Mark where platelets are.
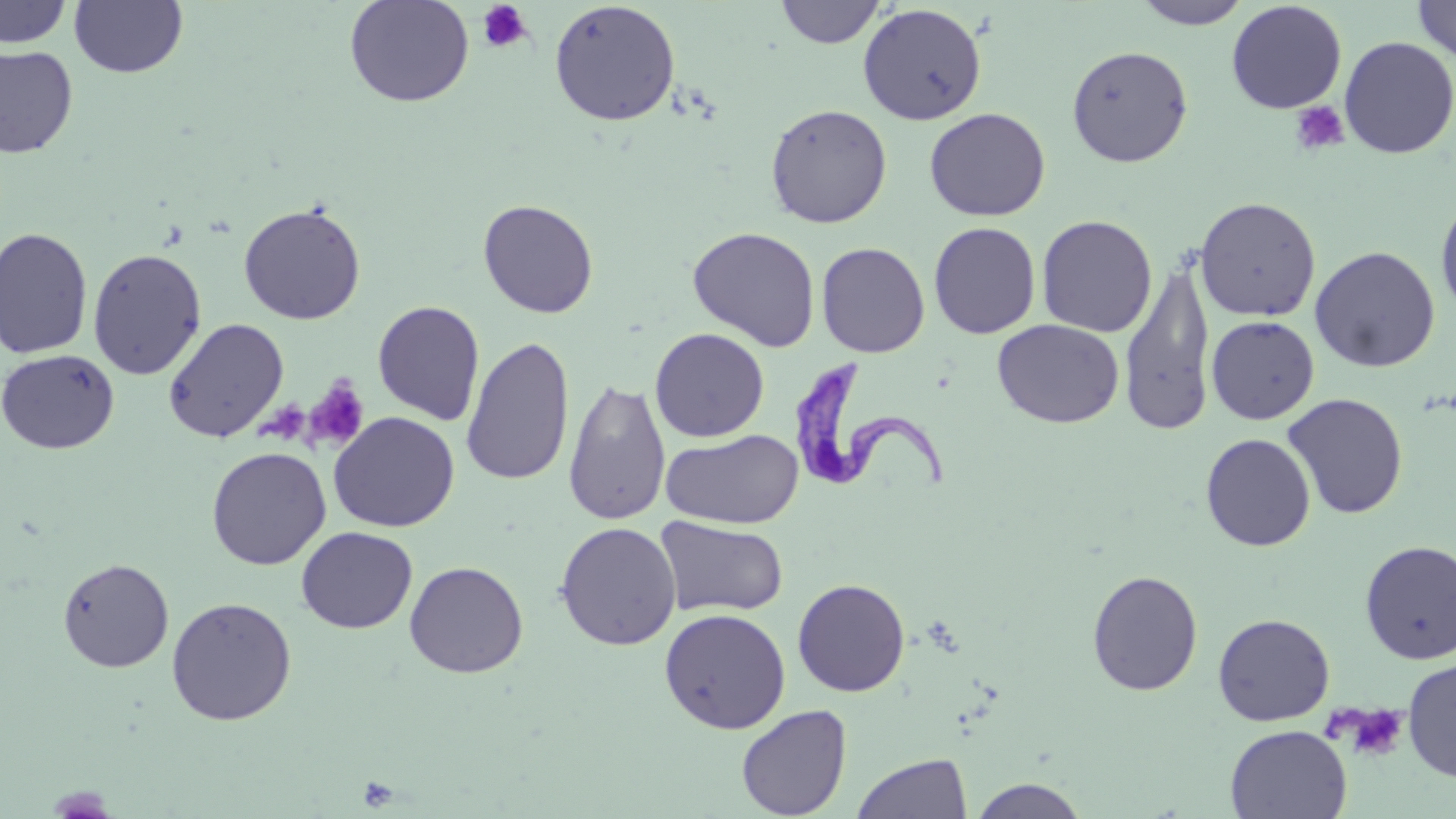

Approximate bounding boxes as [x1, y1, x2, y2] in pixels.
Platelets: [476, 1, 534, 53], [1290, 101, 1350, 156], [303, 378, 370, 452], [1339, 704, 1409, 761].

Summary:
  - Uninfected red blood cell locations: [343, 0, 475, 108], [1131, 0, 1253, 29], [1412, 0, 1456, 64], [0, 1, 73, 49], [69, 1, 188, 78], [549, 1, 680, 127], [775, 1, 886, 48], [1226, 2, 1347, 114], [857, 3, 987, 125], [1338, 36, 1456, 159], [1066, 44, 1193, 167], [0, 45, 79, 159], [765, 103, 892, 228], [924, 107, 1051, 221], [1435, 194, 1456, 320], [1194, 196, 1321, 322], [478, 199, 599, 318], [238, 202, 366, 325], [1036, 214, 1158, 338], [928, 222, 1041, 339], [0, 226, 94, 359], [687, 226, 821, 352], [816, 241, 931, 358], [1309, 246, 1441, 373], [87, 248, 207, 380], [1119, 255, 1217, 436], [372, 300, 485, 426], [1206, 315, 1319, 423], [162, 318, 289, 442], [992, 319, 1125, 429], [649, 328, 769, 443], [461, 336, 575, 487], [0, 348, 120, 454], [562, 377, 670, 526], [1283, 393, 1408, 519], [328, 412, 460, 532], [661, 428, 804, 530], [1200, 433, 1316, 551], [206, 446, 331, 570], [654, 516, 789, 618], [555, 521, 681, 650], [296, 527, 417, 633], [1359, 540, 1456, 665], [57, 557, 175, 672], [404, 560, 528, 678], [1086, 569, 1204, 696], [792, 578, 910, 697], [166, 596, 297, 726], [659, 608, 791, 733], [1212, 613, 1335, 726], [1402, 658, 1456, 781], [736, 704, 852, 818], [1225, 724, 1352, 818], [851, 752, 972, 818], [966, 776, 1091, 818]
  - Trypanosoma brucei locations: [787, 359, 950, 495]
  - Slide-level diagnosis: Trypanosoma brucei
  - Stain: May-Grünwald-Giemsa
  - Preparation: thin blood smear
  - Modality: optical microscopy
  - Field of view: one of a larger specimen
  - Image size: 1456×819 pixels
  - Magnification: 1000x